Report the malaria status of this cell.
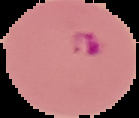

It is parasitized.

From a thin blood film. Cell region segmented out of the field of view; the surrounding area is masked to black. Image is 139×118 pixels.